Assess this cell for malaria.
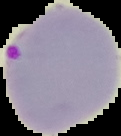
It is parasitized.

Summary:
  - Image size: 121×136 pixels
  - Image type: segmented cell region with the area outside set to black
  - Preparation: thin blood smear